Locate every parasitized red blood cell.
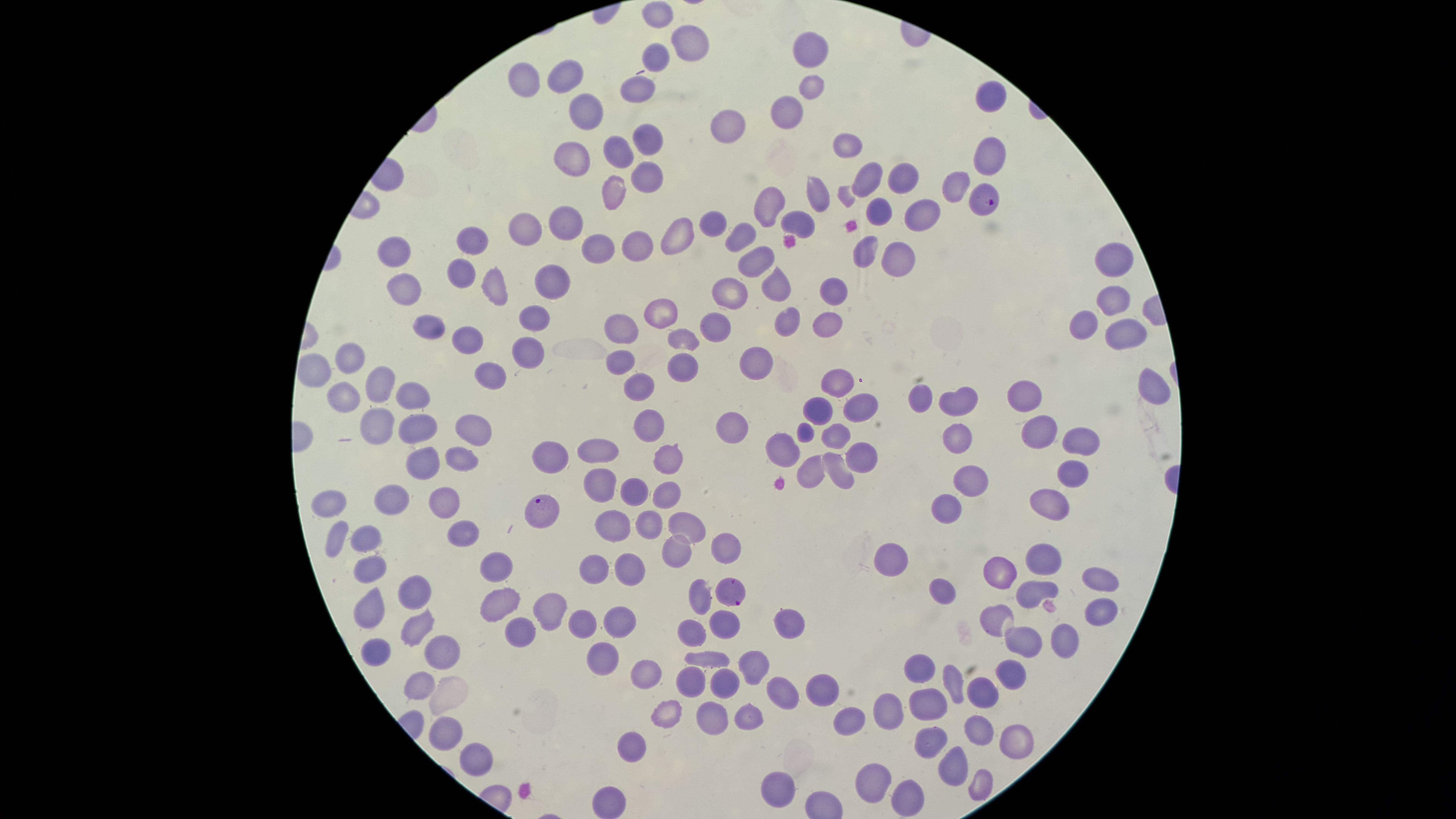

Approximate marker points as [x, y] in pixels.
Parasitized red blood cells: [980, 198], [540, 512], [732, 596].

Approximate marker points as [x, y] in pixels. Uninfected red blood cells: [657, 14], [811, 46], [692, 48], [654, 53], [566, 74], [526, 79], [810, 88], [634, 90], [994, 98], [786, 109], [584, 112], [732, 125], [645, 138], [845, 143], [617, 148], [572, 159], [989, 159], [867, 177], [904, 178], [645, 179], [957, 185], [811, 194], [615, 195], [765, 202], [881, 207], [923, 211], [707, 222], [799, 224], [529, 225], [565, 227], [739, 230], [673, 231], [471, 239], [638, 244], [601, 250], [863, 251], [398, 252], [757, 253], [891, 259], [1108, 263], [463, 270], [771, 281], [406, 282], [553, 282], [496, 287], [834, 288], [734, 291], [1102, 297], [536, 312], [654, 314], [615, 323], [825, 323], [715, 324], [789, 325], [427, 328], [1087, 328], [1120, 329], [686, 336], [464, 337], [533, 354], [345, 359], [615, 361], [761, 363], [686, 367], [314, 374], [494, 374], [839, 377], [376, 381], [633, 381], [1161, 386], [417, 388], [338, 396], [916, 398], [962, 398], [1030, 399], [867, 406], [823, 410], [374, 421], [646, 421], [735, 428], [1036, 428], [472, 432], [949, 432], [1081, 432], [415, 433], [832, 439], [669, 445], [598, 449], [782, 451], [464, 456], [548, 457], [855, 458], [426, 461], [814, 465], [838, 469], [1071, 472], [971, 481], [595, 491], [633, 491], [666, 494], [443, 497], [388, 500], [330, 505], [1043, 505], [948, 506], [649, 525], [460, 529], [620, 529], [688, 529], [369, 533], [335, 537], [672, 550], [722, 550], [1048, 559], [896, 560], [496, 562], [369, 567], [595, 568], [629, 571], [1005, 575], [1097, 578], [410, 584], [1030, 592], [699, 593], [940, 593], [498, 602], [372, 609], [547, 611], [1093, 612], [1003, 617], [580, 620], [618, 620], [724, 621], [415, 622], [785, 628], [690, 631], [517, 633], [1054, 636], [1024, 638], [441, 643], [375, 654], [597, 657], [707, 661], [759, 666], [919, 667], [643, 668], [1011, 673], [957, 678], [725, 679], [693, 681], [420, 685], [980, 687], [816, 689], [783, 692], [925, 699], [892, 708], [747, 713], [668, 718], [707, 719], [845, 719], [449, 730], [976, 733], [926, 743], [1009, 743], [627, 749], [473, 755], [952, 761], [873, 777], [981, 777], [905, 786], [777, 787], [607, 795]. Giemsa stain. Image is 1456×819 pixels. The visible region is circular. Species: Plasmodium falciparum. Smartphone photograph through the microscope eyepiece. Thin blood film. Single field of view.